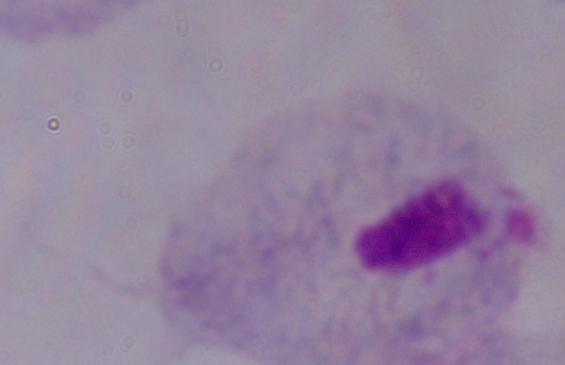 Photomicrograph. A trichomonad is seen. Captured at 1000x magnification.